Comment on the morphology of the erythrocytes.
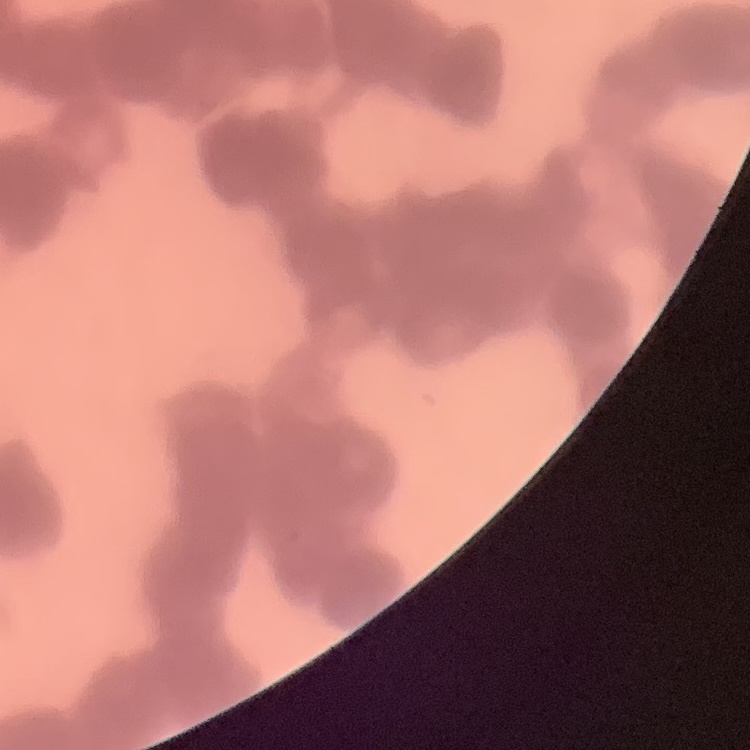

They show rouleaux formation.

{
  "image_type": "one tile cut from a larger photomicrograph",
  "stain": "Field's or Giemsa",
  "preparation": "thin peripheral smear"
}